Name the parasite shown.
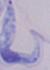
This is a trypanosome.

Photomicrograph. 1000x magnification.